Classify this cell by malaria status.
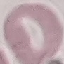
Uninfected.

Summary:
  - Image type: automatically extracted cell patch, resized to 64 × 64 pixels
  - Stain: Giemsa
  - Preparation: thin smear
  - Capture: smartphone camera at the microscope eyepiece